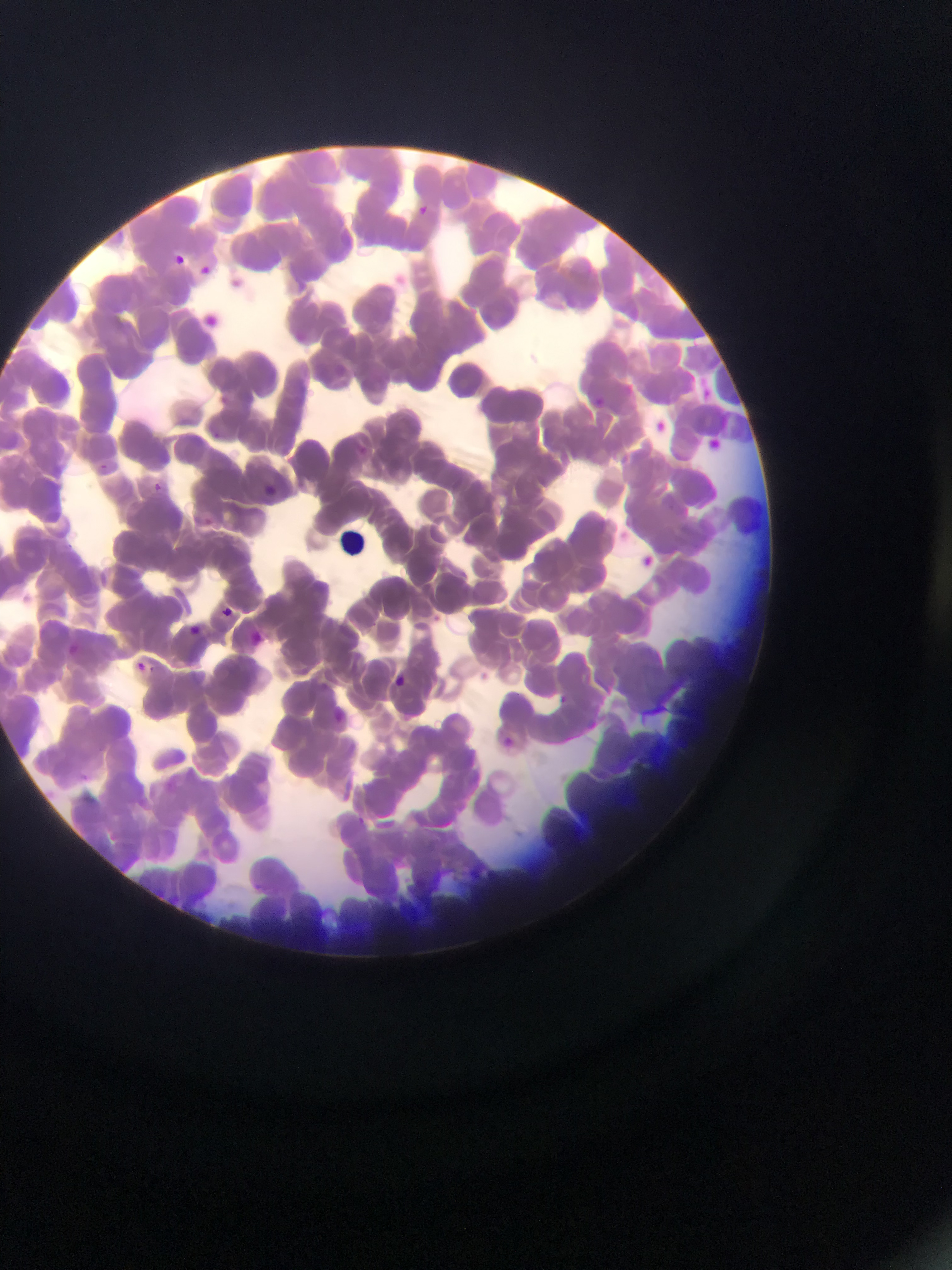

Approximate bounding boxes as left top right bottom in pixels. Plasmodium parasite locations: 412 202 432 223; 173 248 196 263; 201 262 210 275; 699 379 717 406; 592 394 608 412; 651 417 667 439; 704 435 725 453; 152 478 176 496; 259 478 281 494; 222 601 231 621; 181 623 209 635; 251 624 271 648; 65 642 80 656; 135 660 163 676; 388 668 409 688; 332 711 359 732; 504 727 512 751. Photographed through a microscope with a mobile-phone camera. Image is 952×1270 pixels. Sample from Ghana. Single field of view. Thin blood smear.